Classify this cell by malaria status.
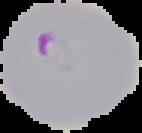

Parasitized.

preparation = thin blood smear
image size = 142×133 pixels
image type = cell region segmented out of the field of view; surrounding area masked to black